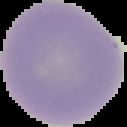
Summary:
  - Image size: 127×127 pixels
  - Image type: segmented cell region with the area outside set to black
  - Result: no malaria parasites seen
  - Preparation: thin blood smear